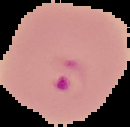
Malaria status: parasitized. Segmented cell region on a black background. From a thin blood film. Image is 130×127 pixels.